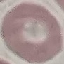
Summary:
  - Result: negative for malaria parasites
  - Preparation: thin blood smear
  - Stain: Giemsa
  - Image type: cell patch, automatically extracted from a larger field of view and resized to 64 × 64 pixels
  - Capture: smartphone through the microscope eyepiece